Assess the morphology of the erythrocytes.
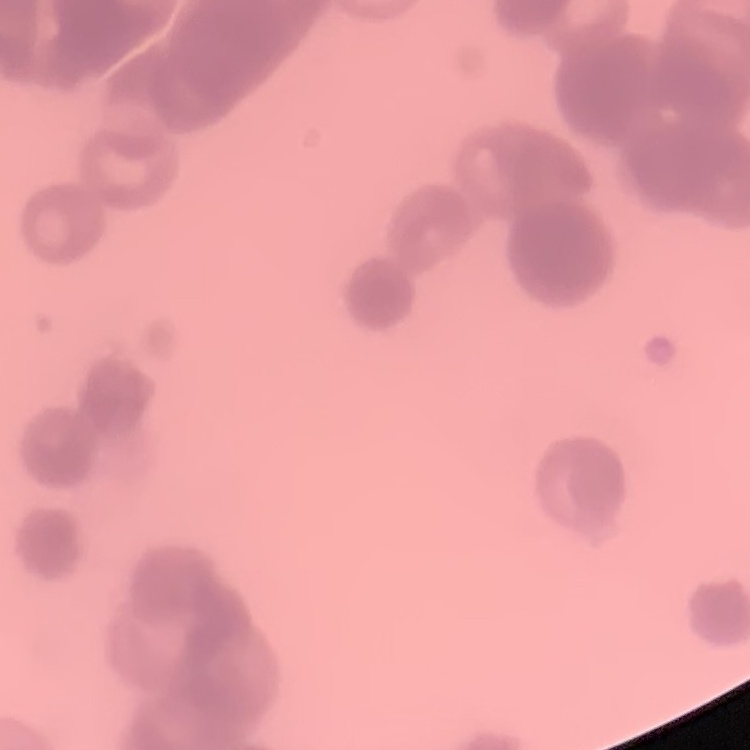

They show rouleaux formation.

Summary:
  - Preparation: thin blood film
  - Image type: one tile cut from a larger photomicrograph
  - Stain: Field's or Giemsa